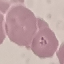
Summary:
  - Result: malaria parasites detected
  - Image type: cell patch, automatically extracted from a larger field of view and resized to 64 × 64 pixels
  - Capture: smartphone through the microscope eyepiece
  - Preparation: thin blood smear
  - Stain: Giemsa